Give the extent of all Plasmodium ovale-infected red blood cells.
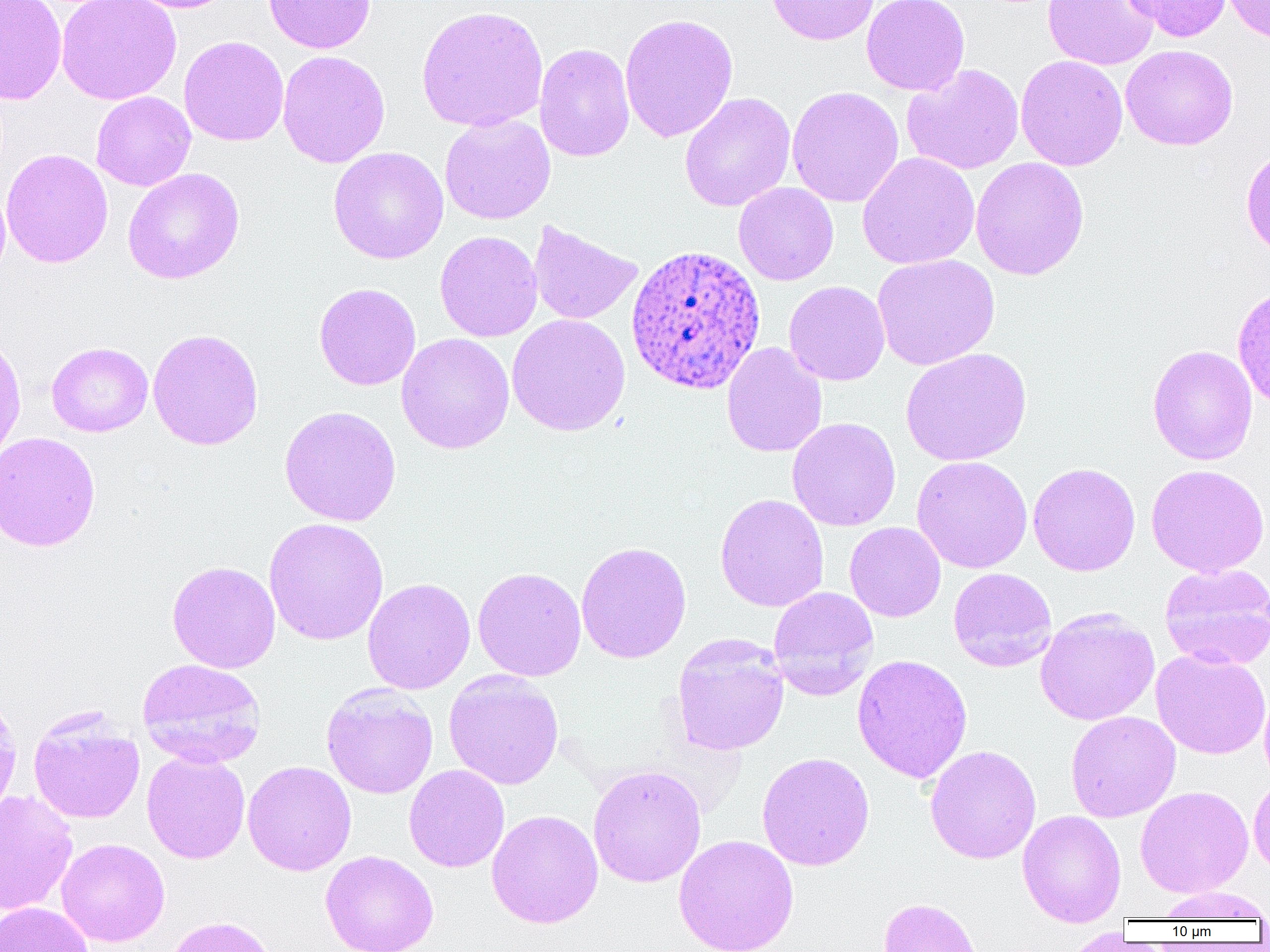

Approximate bounding boxes as [x1, y1, x2, y2] in pixels.
Plasmodium ovale-infected red blood cells: [624, 244, 766, 396].

Uninfected red blood cell locations: [0, 0, 67, 104], [56, 0, 181, 105], [123, 0, 238, 13], [264, 0, 375, 54], [765, 0, 879, 46], [862, 0, 970, 96], [1042, 0, 1159, 70], [1121, 0, 1231, 42], [1221, 0, 1270, 44], [416, 5, 548, 132], [619, 13, 738, 142], [179, 36, 289, 146], [534, 42, 635, 162], [1120, 44, 1238, 150], [277, 50, 390, 168], [1015, 55, 1127, 171], [901, 64, 1024, 175], [786, 85, 904, 207], [91, 91, 196, 191], [679, 92, 796, 212], [439, 114, 556, 225], [1240, 145, 1270, 260], [328, 146, 448, 264], [0, 148, 114, 268], [857, 152, 980, 270], [970, 157, 1089, 280], [122, 168, 244, 284], [733, 182, 838, 285], [527, 220, 643, 325], [434, 230, 543, 342], [872, 254, 1000, 371], [783, 280, 890, 386], [314, 282, 421, 390], [507, 314, 630, 436], [147, 328, 264, 451], [0, 332, 26, 466], [396, 332, 515, 455], [46, 342, 153, 437], [721, 342, 827, 458], [1147, 344, 1258, 465], [899, 347, 1033, 466], [278, 405, 401, 527], [787, 417, 901, 531], [0, 431, 101, 552], [911, 455, 1033, 573], [1028, 462, 1140, 576], [1146, 464, 1269, 577], [715, 493, 829, 613], [264, 517, 389, 646], [845, 522, 946, 622], [576, 541, 692, 663], [167, 560, 281, 673], [1159, 564, 1270, 670], [472, 567, 586, 682], [947, 567, 1057, 672], [362, 578, 475, 695], [768, 586, 880, 699], [1034, 608, 1160, 726], [672, 634, 790, 756], [1151, 649, 1270, 759], [851, 653, 973, 784], [137, 658, 267, 769], [443, 669, 564, 790], [1259, 682, 1270, 789], [320, 684, 439, 799], [0, 693, 23, 820], [1065, 710, 1181, 822], [28, 711, 144, 824], [925, 744, 1041, 864], [142, 751, 251, 864], [756, 751, 875, 871], [243, 760, 357, 876], [587, 764, 707, 888], [403, 765, 509, 872], [1248, 772, 1270, 877], [1135, 786, 1254, 897], [0, 790, 78, 916], [486, 809, 603, 928], [1017, 809, 1126, 927], [674, 834, 799, 952], [56, 838, 170, 946], [320, 851, 439, 952], [1153, 886, 1270, 921], [877, 897, 984, 952], [0, 901, 92, 952], [162, 915, 279, 952], [1062, 926, 1128, 952]. Slide-level diagnosis: Plasmodium ovale. Optical microscopy. Captured at 1000x magnification. Image is 1270×952 pixels. One field of a larger specimen. Thin blood film.